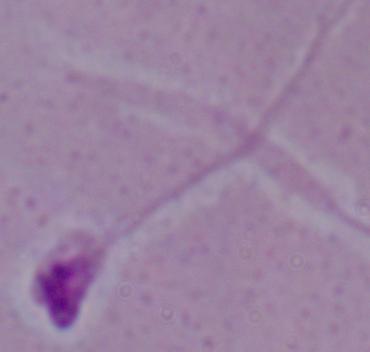 A Leishmania parasite is shown. Photomicrograph. 1000x magnification.